Classify this cell by malaria status.
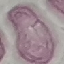

It is uninfected.

Thin smear of blood. Giemsa-stained preparation. Cell patch, automatically extracted from a larger field of view and resized to 64 × 64 pixels. Acquired by smartphone through the microscope eyepiece.